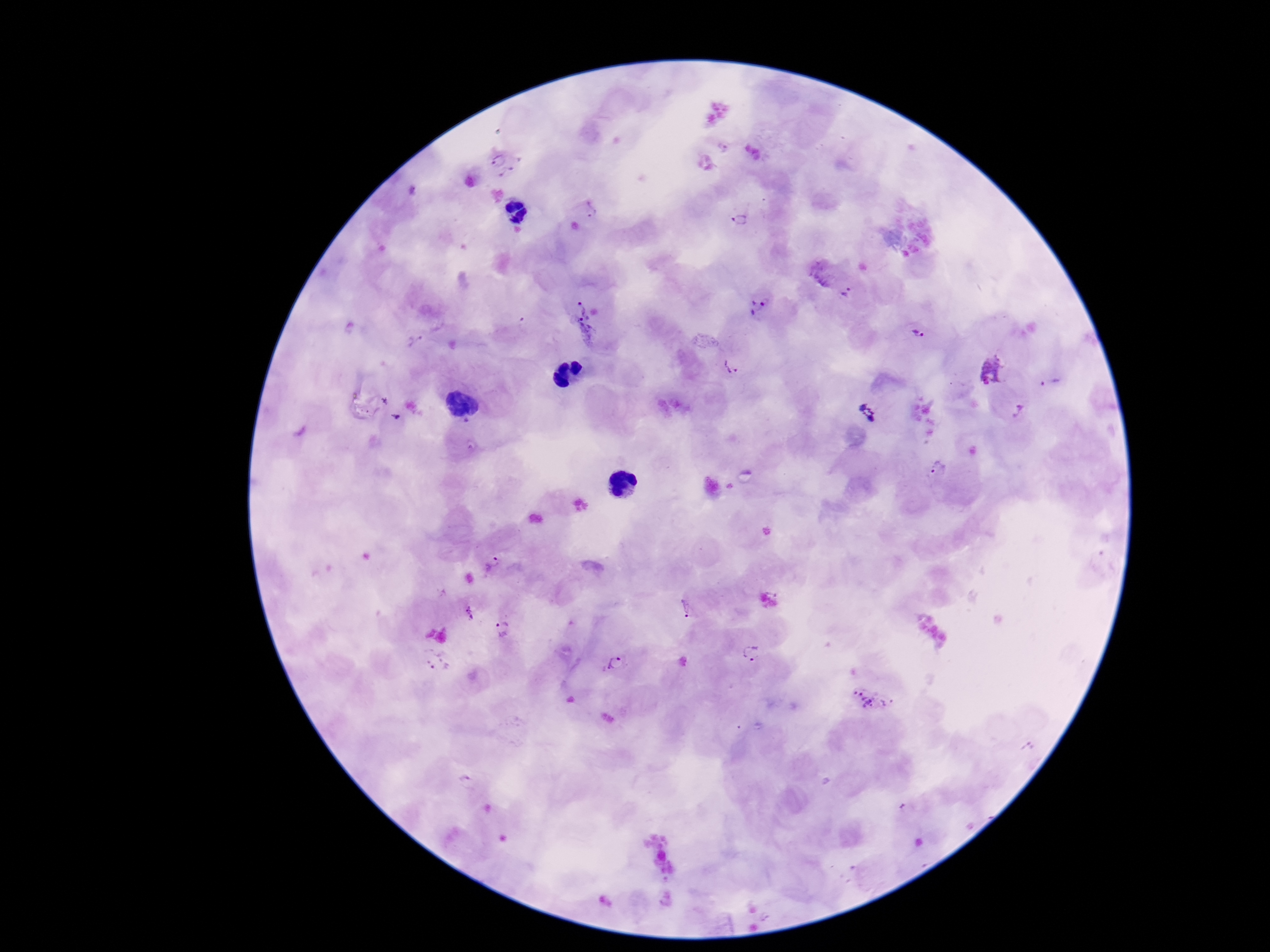

Approximate object centers, in pixels from the top-left corner.
Summary:
  - Plasmodium parasite locations: (x=504, y=164), (x=591, y=209), (x=739, y=218), (x=847, y=293), (x=759, y=307), (x=583, y=321), (x=918, y=335), (x=417, y=342), (x=731, y=367), (x=991, y=374), (x=1051, y=380), (x=867, y=411), (x=1018, y=411), (x=937, y=471), (x=493, y=561), (x=685, y=610), (x=468, y=614), (x=504, y=630), (x=751, y=654), (x=437, y=664), (x=613, y=664), (x=870, y=700), (x=466, y=781), (x=904, y=809)
  - Magnification: 100x
  - Stain: Giemsa
  - Preparation: thick blood smear
  - Patient malaria status: infected
  - Field of view: one from this slide
  - Capture: smartphone camera through the microscope eyepiece
  - Image size: 1270×952 pixels